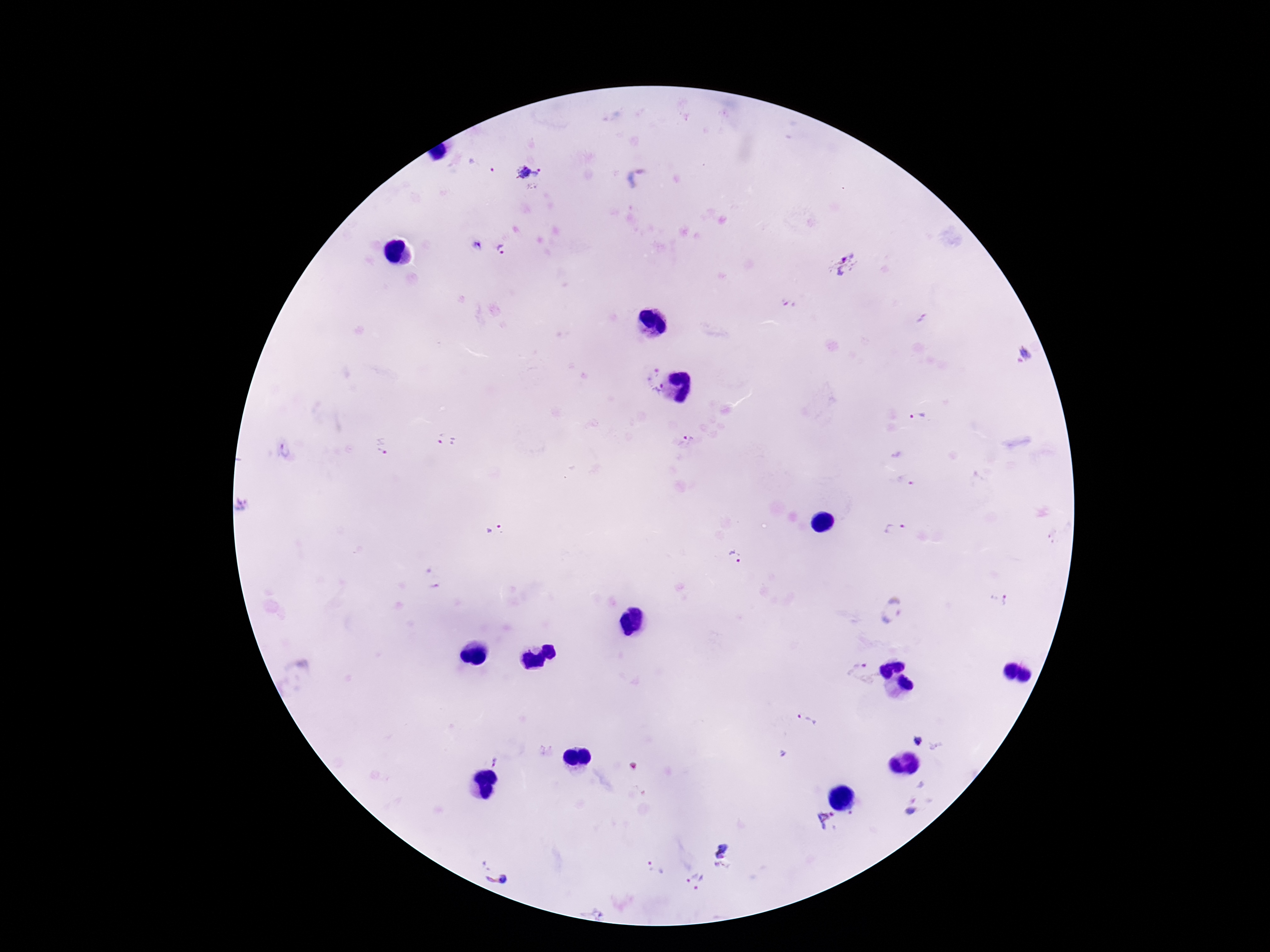
patient_malaria_status: infected
preparation: thick peripheral-blood smear
image_size: 1270×952 pixels
field_of_view: single
magnification: 100x
plasmodium_parasite_locations: 'approximate object centers, in pixels from the top-left corner: (x=483, y=165), (x=529, y=173), (x=638, y=179), (x=502, y=249), (x=845, y=266), (x=789, y=302), (x=1020, y=356), (x=651, y=372), (x=658, y=392), (x=919, y=418), (x=447, y=440), (x=689, y=442), (x=383, y=447), (x=286, y=450), (x=242, y=506), (x=895, y=530), (x=496, y=532), (x=735, y=557), (x=999, y=599), (x=892, y=610), (x=861, y=674), (x=807, y=721), (x=917, y=740), (x=494, y=762), (x=921, y=785), (x=911, y=807), (x=827, y=820), (x=722, y=849), (x=654, y=868), (x=721, y=870), (x=498, y=874), (x=695, y=879)'
stain: Giemsa
capture: smartphone camera through the microscope eyepiece